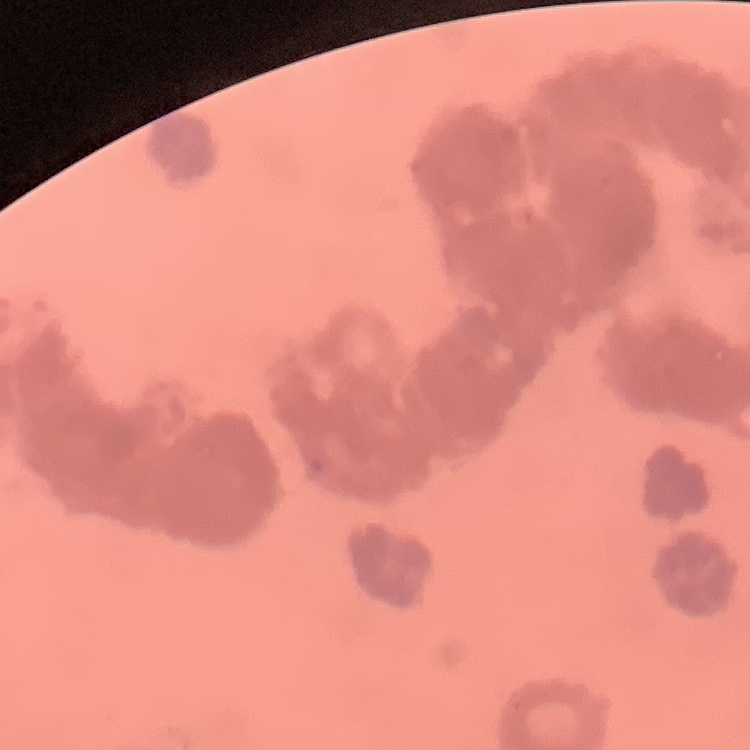

Summary:
  - Red blood cell morphology: rouleaux formation
  - Preparation: thin peripheral smear
  - Image type: square crop of a larger photomicrograph
  - Stain: Field's or Giemsa